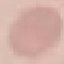

malaria_status: uninfected
capture: smartphone camera at the microscope eyepiece
image_type: automatically extracted cell patch, resized to 64 × 64 pixels
preparation: thin smear
stain: Giemsa